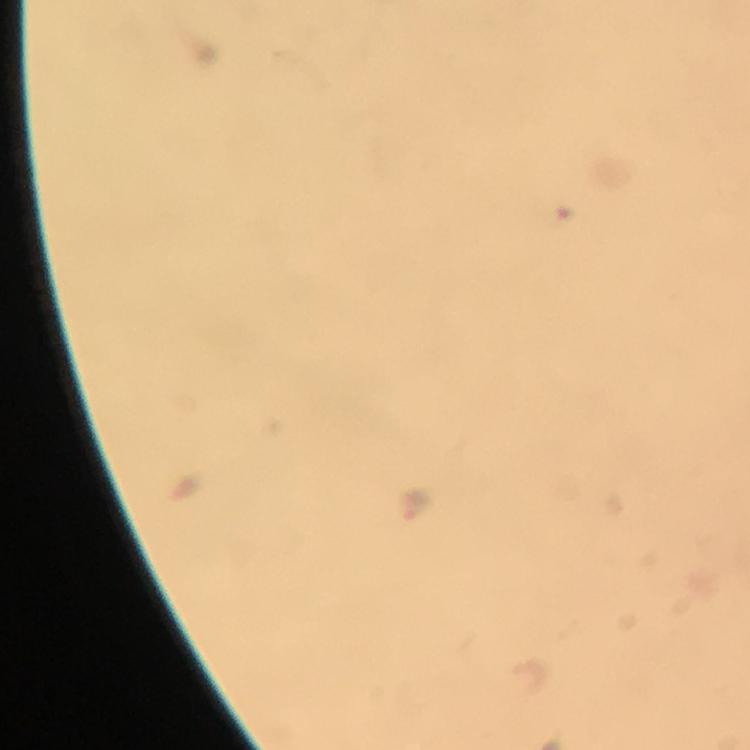
Approximate centers as [x, y] in pixels. Malaria parasite locations: [415, 504]. A crop from one field of view. Smartphone photograph taken through a microscope. Image is 750×750 pixels. Giemsa stain. Immersion oil was used. From a malaria diagnostic workup. Thick smear. 100x magnification.